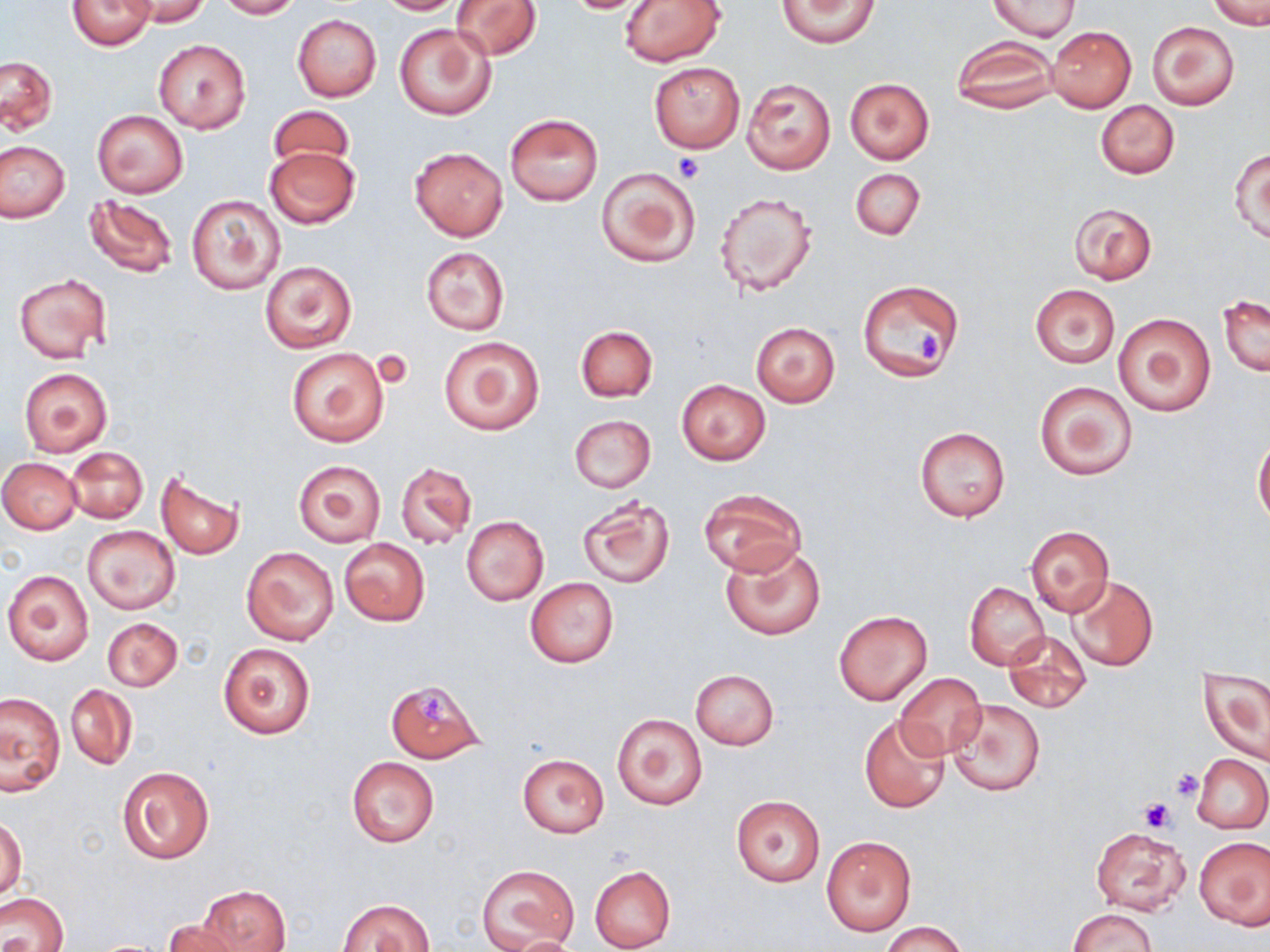

Summary:
  - Coordinate format: approximate bounding boxes as [x1, y1, x2, y2] in pixels
  - Platelet locations: [673, 155, 703, 184], [912, 326, 940, 364], [421, 695, 453, 723], [1169, 768, 1204, 800], [1138, 797, 1176, 832]
  - Uninfected red blood cell locations: [67, 0, 157, 51], [126, 0, 211, 27], [215, 0, 300, 19], [374, 0, 463, 15], [451, 0, 543, 60], [557, 0, 659, 14], [620, 0, 726, 67], [777, 0, 880, 48], [988, 0, 1080, 40], [1208, 1, 1270, 28], [292, 14, 382, 103], [394, 22, 497, 122], [1147, 22, 1239, 110], [1047, 26, 1136, 111], [154, 39, 251, 135], [952, 39, 1058, 113], [0, 56, 58, 134], [649, 61, 744, 152], [742, 78, 835, 174], [845, 78, 935, 165], [1096, 100, 1179, 179], [267, 106, 356, 173], [92, 110, 188, 197], [505, 113, 603, 204], [0, 142, 70, 222], [265, 146, 360, 230], [410, 146, 507, 240], [1230, 146, 1270, 242], [595, 166, 701, 267], [851, 167, 924, 240], [714, 190, 819, 298], [185, 193, 285, 295], [85, 194, 178, 279], [1068, 202, 1157, 285], [421, 247, 509, 335], [259, 261, 356, 353], [14, 274, 111, 362], [858, 279, 965, 382], [1029, 283, 1121, 369], [1218, 294, 1269, 376], [1112, 313, 1215, 417], [751, 321, 839, 407], [575, 324, 657, 403], [439, 335, 544, 435], [285, 347, 391, 448], [20, 368, 112, 456], [676, 379, 770, 465], [1034, 380, 1137, 481], [569, 415, 656, 492], [915, 427, 1010, 521], [1254, 436, 1270, 526], [65, 447, 148, 523], [1, 458, 81, 534], [293, 460, 385, 547], [396, 462, 476, 548], [155, 469, 246, 559], [699, 489, 806, 577], [576, 494, 675, 588], [461, 516, 548, 605], [1024, 525, 1115, 619], [83, 526, 179, 613], [338, 537, 431, 627], [720, 542, 825, 641], [242, 546, 339, 645], [3, 569, 94, 666], [1068, 575, 1158, 672], [524, 579, 618, 668], [964, 582, 1049, 669], [833, 610, 933, 706], [102, 617, 182, 691], [1003, 630, 1091, 713], [219, 642, 316, 739], [1199, 666, 1270, 766], [691, 669, 778, 750], [894, 671, 986, 760], [385, 678, 486, 763], [65, 685, 137, 770], [1, 691, 65, 794], [948, 698, 1046, 798], [610, 713, 709, 812], [859, 714, 950, 812], [516, 754, 609, 837], [1193, 754, 1270, 834], [346, 756, 439, 848], [117, 764, 215, 863], [732, 796, 824, 886], [0, 817, 25, 901], [1090, 826, 1189, 915], [821, 836, 915, 935], [1195, 837, 1269, 930], [477, 863, 580, 951], [590, 865, 675, 950], [199, 885, 292, 952], [0, 892, 68, 952], [338, 897, 434, 951], [1068, 907, 1156, 952], [163, 918, 245, 952], [880, 921, 966, 952], [500, 935, 589, 952]
  - Slide-level diagnosis: negative for blood parasites
  - Magnification: 1000x
  - Stain: May-Grünwald-Giemsa
  - Image size: 1270×952 pixels
  - Preparation: thin blood film
  - Modality: light microscopy
  - Field of view: one of a larger specimen